Outline each blood parasite and name the species.
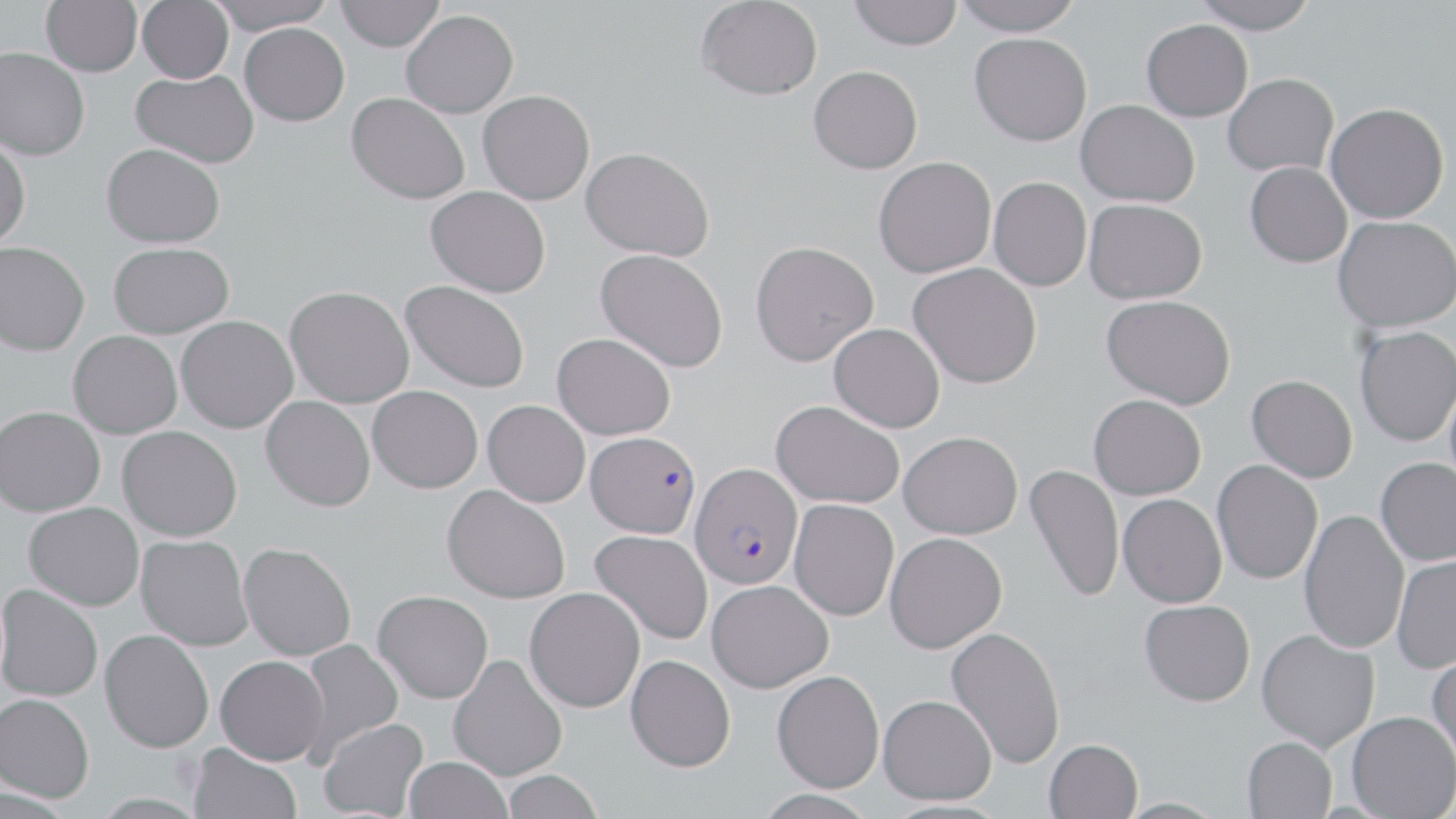
Approximate bounding boxes as (x1, y1, x2, y2) in pixels.
Plasmodium falciparum-infected red blood cells: (585, 431, 700, 538), (689, 462, 803, 589).
No Plasmodium ovale, Plasmodium malariae, Plasmodium vivax, Babesia divergens, or Trypanosoma brucei observed.

{
  "slide_level_diagnosis": "Plasmodium falciparum",
  "stain": "May-Grünwald-Giemsa",
  "field_of_view": "single",
  "uninfected_red_blood_cell_locations": "approximate bounding boxes as (x1, y1, x2, y2) in pixels: (41, 0, 142, 76), (137, 0, 234, 84), (205, 0, 338, 35), (334, 0, 444, 51), (696, 0, 823, 100), (849, 0, 962, 51), (951, 0, 1084, 35), (1192, 0, 1320, 34), (401, 9, 518, 118), (1142, 19, 1253, 121), (240, 23, 350, 126), (969, 33, 1092, 146), (0, 47, 90, 161), (809, 65, 922, 173), (131, 69, 258, 168), (1223, 73, 1338, 176), (478, 89, 595, 205), (347, 92, 470, 204), (1076, 99, 1200, 207), (1325, 102, 1449, 223), (0, 138, 30, 249), (101, 143, 225, 248), (581, 146, 715, 261), (873, 156, 996, 278), (1245, 161, 1352, 267), (989, 176, 1092, 291), (425, 186, 551, 297), (1084, 198, 1207, 304), (1333, 215, 1456, 333), (749, 240, 879, 366), (0, 241, 90, 356), (109, 242, 235, 339), (595, 248, 728, 373), (909, 262, 1042, 389), (400, 280, 531, 393), (285, 286, 415, 408), (1102, 294, 1236, 409), (176, 315, 298, 433), (829, 323, 945, 432), (1355, 326, 1456, 446), (68, 330, 182, 439), (552, 332, 675, 440), (1444, 373, 1456, 496), (1247, 375, 1358, 482), (368, 386, 482, 493), (1089, 394, 1206, 499), (261, 396, 375, 511), (483, 400, 590, 507), (771, 400, 904, 508), (0, 405, 105, 516), (117, 425, 242, 541), (899, 431, 1022, 539), (1375, 457, 1456, 566), (1212, 460, 1323, 584), (1024, 463, 1125, 602), (442, 484, 571, 604), (1118, 494, 1227, 607), (789, 498, 899, 621), (24, 502, 144, 610), (1298, 509, 1409, 654), (590, 530, 712, 645), (885, 532, 1007, 653), (136, 534, 253, 651), (238, 542, 356, 661), (1392, 555, 1456, 673), (707, 578, 834, 692), (0, 584, 103, 701), (524, 587, 645, 712), (373, 590, 493, 703), (1139, 599, 1255, 706), (946, 626, 1066, 769), (100, 629, 214, 752), (1256, 629, 1379, 751), (296, 639, 404, 761), (1426, 650, 1456, 773), (447, 653, 568, 781), (626, 654, 736, 771), (215, 655, 329, 765), (772, 669, 884, 792), (0, 693, 94, 802), (878, 694, 996, 804), (1346, 711, 1456, 819), (317, 718, 429, 819), (1242, 736, 1337, 818), (1044, 739, 1143, 819), (188, 742, 302, 819), (403, 756, 512, 819), (501, 770, 603, 819)",
  "magnification": "1000x",
  "preparation": "thin blood film",
  "image_size": "1456×819 pixels",
  "modality": "optical microscopy"
}